State the blood parasite species.
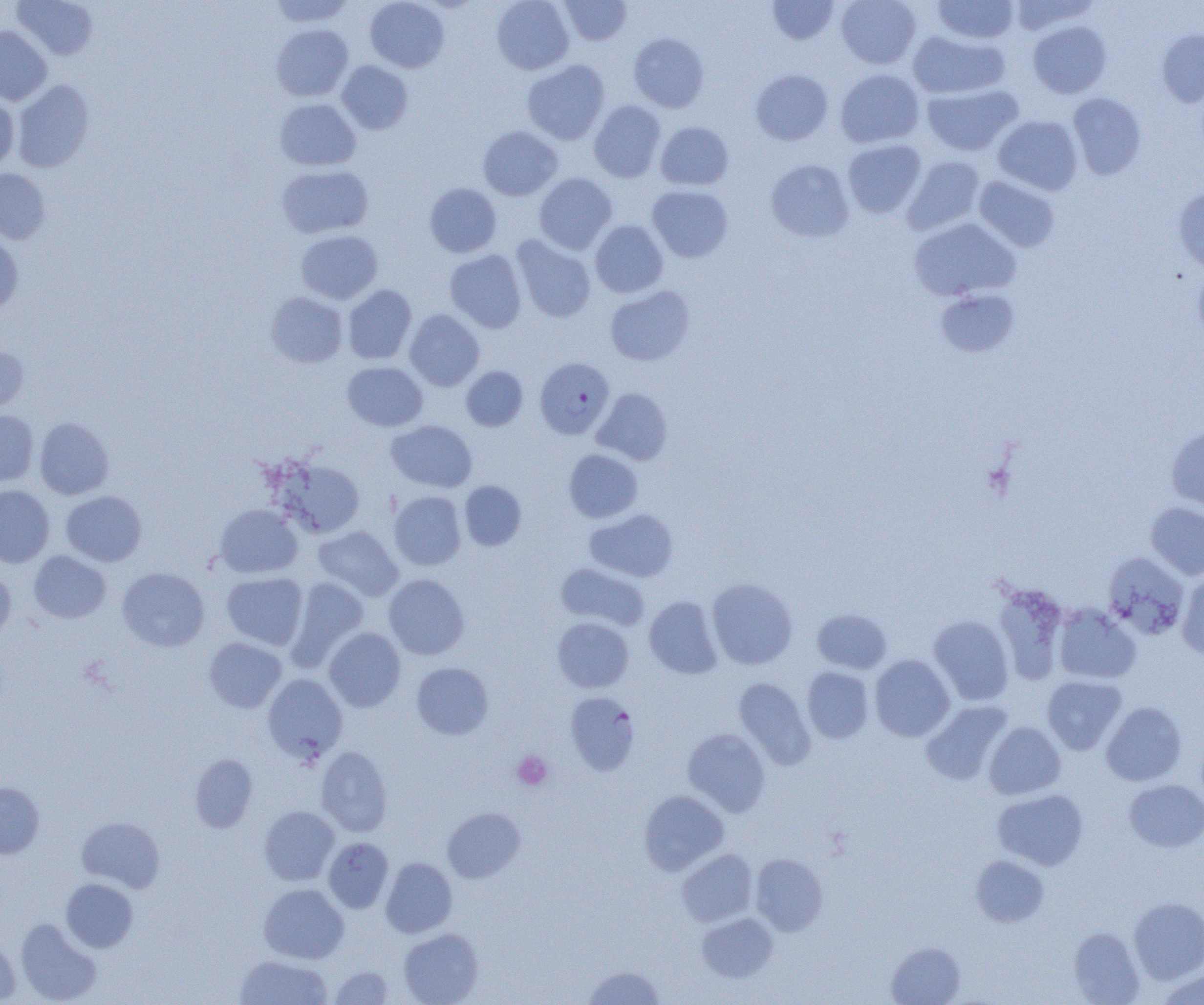
Plasmodium falciparum.

Approximate bounding boxes as (x1,y1)-(x2,y2) corner pairs in pixels. Plasmodium falciparum-infected red blood cell locations: (535,356)-(615,438). Platelet locations: (512,751)-(553,790). Uninfected red blood cell locations: (13,0)-(99,60), (267,0)-(355,27), (365,0)-(450,73), (492,0)-(574,75), (560,0)-(632,46), (767,0)-(840,45), (836,0)-(920,69), (933,0)-(1019,44), (1008,0)-(1100,34), (1027,21)-(1112,98), (271,24)-(353,102), (0,26)-(52,105), (908,29)-(1010,99), (1157,29)-(1204,107), (628,33)-(709,112), (336,60)-(413,134), (522,60)-(610,145), (751,68)-(833,145), (835,69)-(925,148), (12,79)-(95,173), (922,83)-(1023,155), (1068,92)-(1147,180), (0,96)-(19,171), (274,98)-(361,171), (589,100)-(665,182), (992,115)-(1083,195), (655,121)-(734,190), (477,125)-(563,200), (842,139)-(926,218), (902,156)-(985,235), (766,159)-(854,242), (277,164)-(374,238), (0,168)-(51,244), (534,172)-(617,254), (974,175)-(1060,252), (424,183)-(501,258), (647,185)-(733,262), (1173,187)-(1204,273), (909,217)-(1020,302), (590,219)-(668,298), (296,229)-(383,304), (0,233)-(24,318), (511,235)-(597,323), (445,250)-(527,333), (1193,266)-(1204,346), (342,284)-(416,364), (604,285)-(695,365), (935,289)-(1020,357), (266,291)-(348,368), (404,309)-(484,391), (0,345)-(30,414), (342,361)-(428,431), (461,366)-(528,431), (592,388)-(673,465), (0,409)-(39,486), (34,417)-(114,500), (386,420)-(477,492), (1165,425)-(1204,512), (564,449)-(643,522), (274,457)-(366,539), (459,481)-(526,550), (0,485)-(55,567), (61,490)-(147,566), (389,491)-(467,571), (1146,501)-(1204,580), (214,504)-(303,577), (584,509)-(679,582), (313,526)-(403,601), (28,550)-(111,623), (1103,551)-(1190,640), (555,562)-(650,631), (117,567)-(210,652), (0,568)-(16,643), (221,572)-(308,650), (1177,572)-(1204,658), (383,574)-(470,659), (286,576)-(369,670), (706,578)-(797,670), (992,583)-(1069,685), (644,596)-(723,679), (1053,604)-(1141,684), (812,608)-(892,673), (929,615)-(1014,705), (552,617)-(634,692), (324,627)-(406,712), (204,637)-(287,713), (869,655)-(955,741), (411,662)-(494,740), (802,666)-(874,744), (262,674)-(348,762), (1041,676)-(1127,754), (733,677)-(816,770), (564,692)-(640,776), (921,701)-(1012,784), (1101,702)-(1187,786), (984,722)-(1066,799), (682,728)-(771,817), (316,747)-(393,836), (190,754)-(258,833), (1124,779)-(1204,852), (0,782)-(44,859), (992,789)-(1089,870), (638,790)-(729,875), (259,806)-(339,886), (443,807)-(524,882), (76,817)-(165,892), (323,837)-(394,913), (677,849)-(757,926), (750,854)-(828,935), (971,855)-(1050,927), (380,857)-(457,938), (61,877)-(138,952), (258,883)-(349,964), (1129,897)-(1204,983), (696,912)-(777,982), (15,917)-(102,1004), (1068,927)-(1145,1004), (398,928)-(483,1005), (0,936)-(20,1004), (885,942)-(966,1005), (234,955)-(333,1005), (581,965)-(666,1005), (328,966)-(394,1004), (1156,967)-(1204,1005). Captured at 1000x magnification. One field of a larger specimen. Thin blood smear. Image is 1204×1005 pixels. Light microscopy.